Evaluate for parasitized red blood cells.
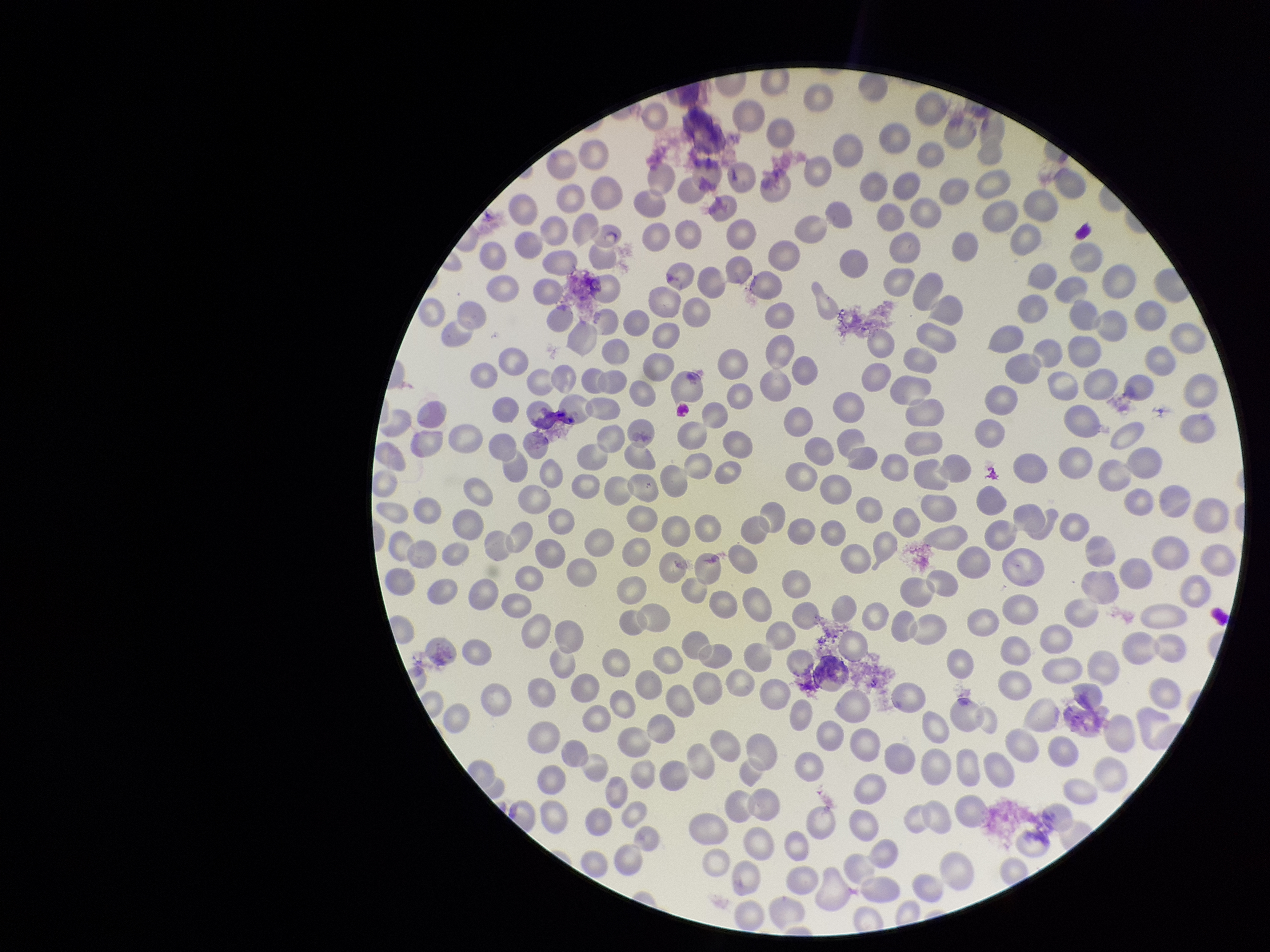

None identified.

Red blood cell count: 293. Preparation: thin blood smear. Giemsa stain. Photographed through the microscope eyepiece with a smartphone camera. Image is 1270×952 pixels. Patient malaria status: negative. One field from this slide. Parasitized red blood cell count: 0.